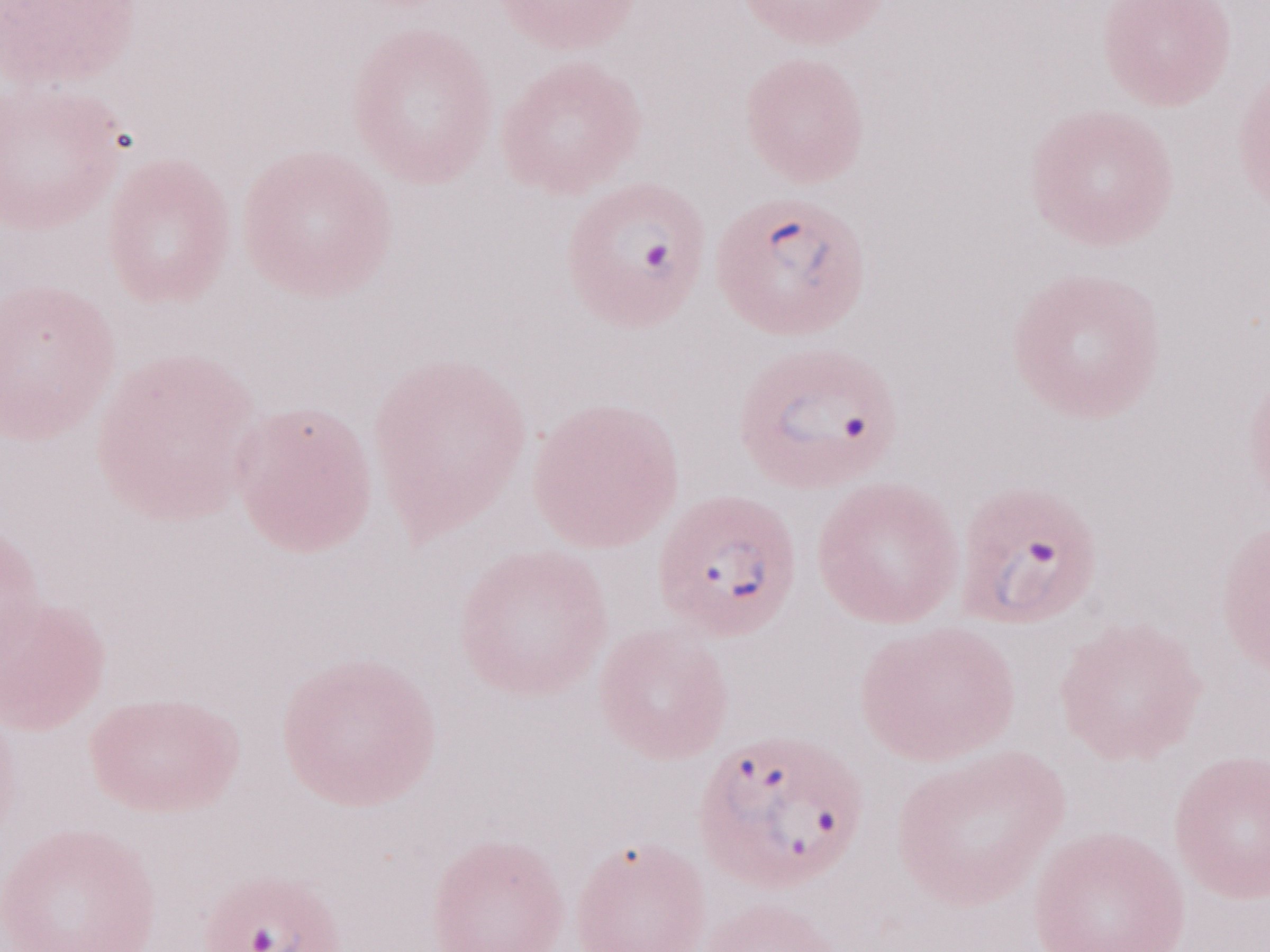 Malaria diagnosis (patient-level): positive. May-Grünwald-Giemsa stain. Olympus BX43 microscope and DP73 digital camera. Thin blood smear. Single field of view. Image is 1270×952 pixels. Magnification: 1,000x.